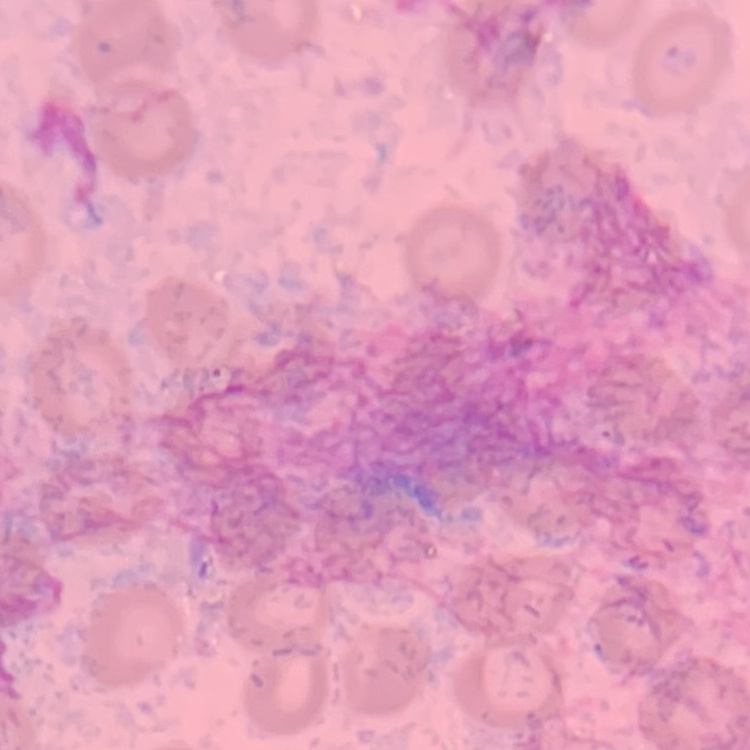
The red blood cells show no rouleaux formation. Square crop of a larger photomicrograph. Field's or Giemsa stain. Thin peripheral smear.